State the blood parasite species.
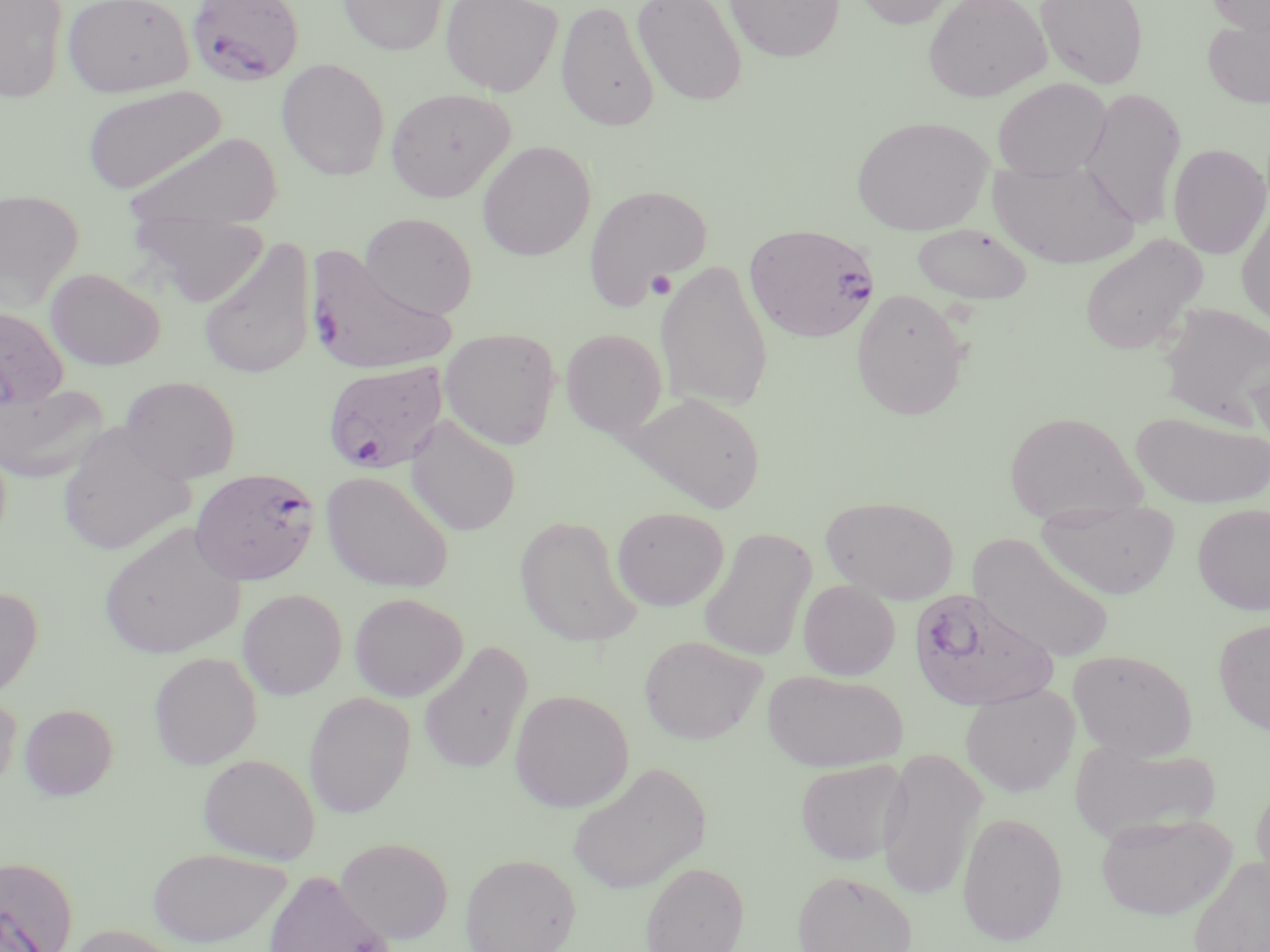

Plasmodium falciparum.

Approximate bounding boxes as [x1, y1, x2, y2] in pixels. Platelet locations: [646, 269, 678, 299]. Plasmodium falciparum-infected red blood cell locations: [186, 0, 303, 86], [744, 223, 881, 342], [303, 245, 459, 375], [323, 361, 449, 473], [189, 467, 322, 586], [907, 588, 1056, 711], [0, 853, 78, 952]. Uninfected red blood cell locations: [0, 0, 69, 102], [62, 0, 195, 98], [338, 0, 448, 55], [440, 0, 562, 96], [724, 0, 845, 63], [850, 0, 960, 29], [923, 0, 1051, 102], [1035, 0, 1149, 89], [1206, 0, 1270, 34], [556, 1, 659, 132], [631, 1, 748, 108], [1203, 16, 1270, 110], [276, 58, 390, 180], [993, 78, 1112, 181], [81, 84, 225, 195], [385, 87, 515, 203], [1079, 88, 1187, 230], [851, 116, 992, 235], [123, 132, 284, 231], [477, 141, 596, 261], [1167, 143, 1270, 260], [988, 157, 1139, 269], [583, 184, 711, 308], [0, 188, 84, 309], [1236, 203, 1270, 330], [360, 212, 478, 319], [130, 213, 268, 307], [911, 223, 1033, 304], [1079, 233, 1208, 355], [198, 238, 314, 379], [655, 259, 774, 413], [45, 267, 165, 370], [850, 288, 971, 421], [1156, 301, 1270, 428], [0, 305, 69, 409], [440, 328, 561, 450], [560, 328, 668, 440], [118, 376, 241, 483], [0, 383, 107, 484], [626, 391, 765, 513], [1130, 409, 1269, 509], [1004, 410, 1143, 523], [406, 416, 521, 536], [56, 423, 194, 558], [321, 470, 454, 593], [821, 496, 959, 604], [1035, 502, 1180, 600], [1192, 503, 1270, 614], [611, 506, 729, 611], [514, 515, 643, 647], [99, 522, 245, 660], [698, 527, 816, 662], [968, 533, 1116, 664], [798, 579, 900, 680], [0, 585, 43, 702], [237, 588, 347, 700], [349, 593, 467, 702], [1213, 618, 1270, 736], [639, 634, 768, 745], [418, 640, 533, 774], [1067, 648, 1198, 760], [149, 652, 262, 769], [762, 669, 907, 772], [960, 684, 1079, 796], [509, 689, 633, 812], [0, 691, 22, 795], [303, 692, 416, 818], [19, 703, 118, 800], [1070, 739, 1222, 844], [876, 748, 987, 900], [197, 753, 320, 864], [795, 758, 909, 865], [566, 761, 712, 895], [1250, 781, 1270, 896], [957, 811, 1068, 946], [1095, 812, 1236, 920], [335, 836, 454, 944], [146, 847, 292, 948], [460, 853, 581, 952], [1188, 856, 1270, 952], [640, 861, 749, 952], [262, 869, 398, 952], [792, 870, 917, 952], [65, 924, 190, 952]. 1000x magnification. One field of a larger specimen. Image is 1270×952 pixels. Light microscopy. Thin blood film. May-Grünwald-Giemsa-stained preparation.